State the preparation type.
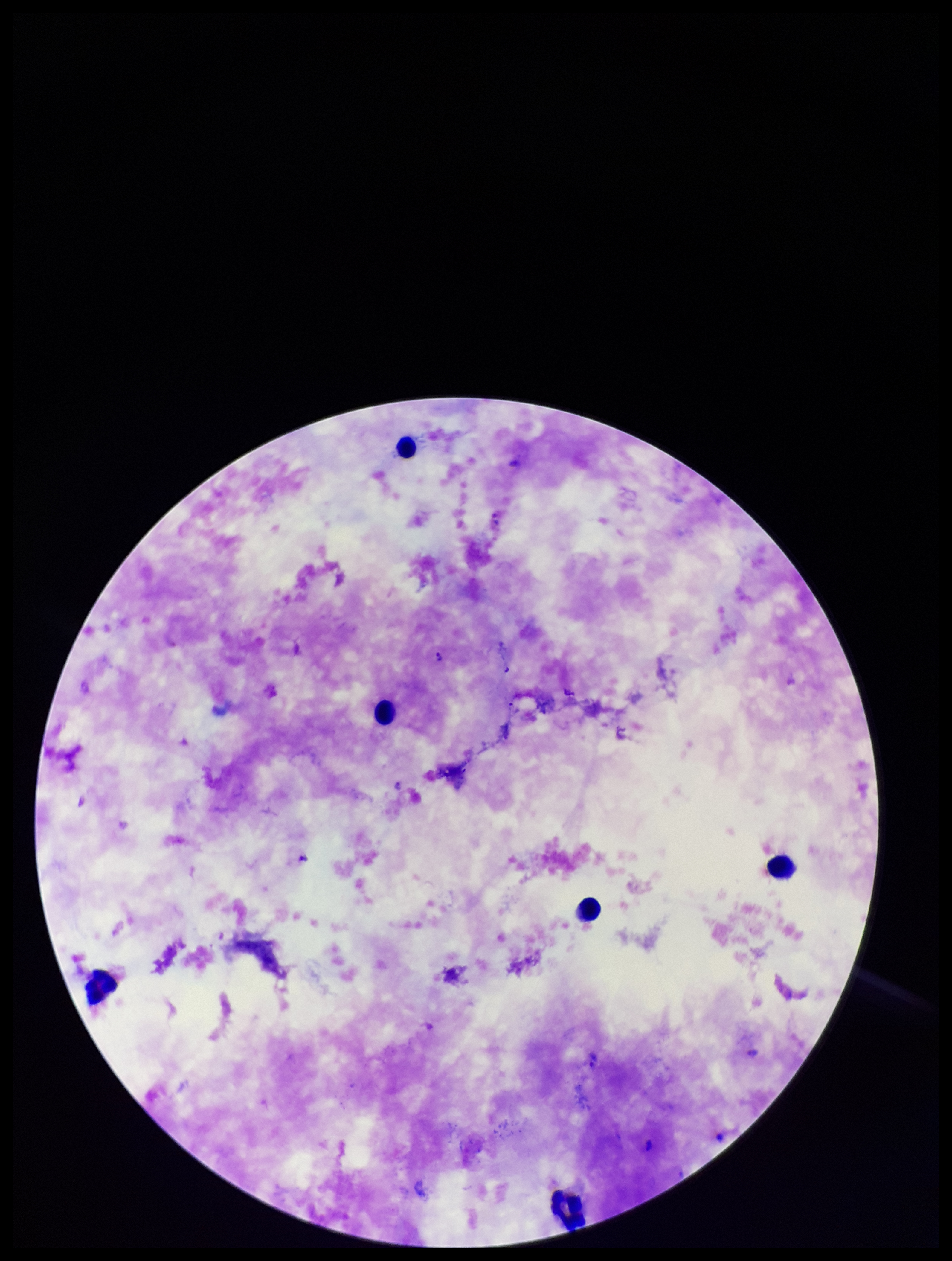

It is a thick blood smear.

Summary:
  - Image size: 952×1261 pixels
  - Plasmodium parasites: identified
  - Stain: Giemsa
  - Patient malaria status: infected
  - Field of view: single
  - Species reported for this patient: Plasmodium falciparum
  - Leukocyte count: 6
  - Parasite count: 4
  - Capture: smartphone photograph through the microscope eyepiece